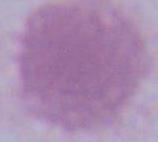

identification = red blood cell
modality = photomicrograph
magnification = 1000x